Assess this cell for malaria.
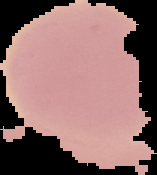
Uninfected.

image_type: segmented cell region on a black background
preparation: thin blood smear
image_size: 157×175 pixels